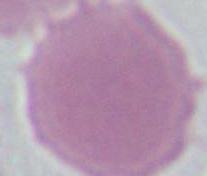
modality = photomicrograph
magnification = 1000x
identification = red blood cell